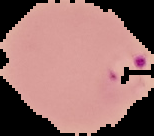
Summary:
  - Image size: 154×136 pixels
  - Preparation: thin blood smear
  - Image type: cell region segmented out of the field of view; surrounding area masked to black
  - Result: malaria parasites detected